Identify the blood parasite species.
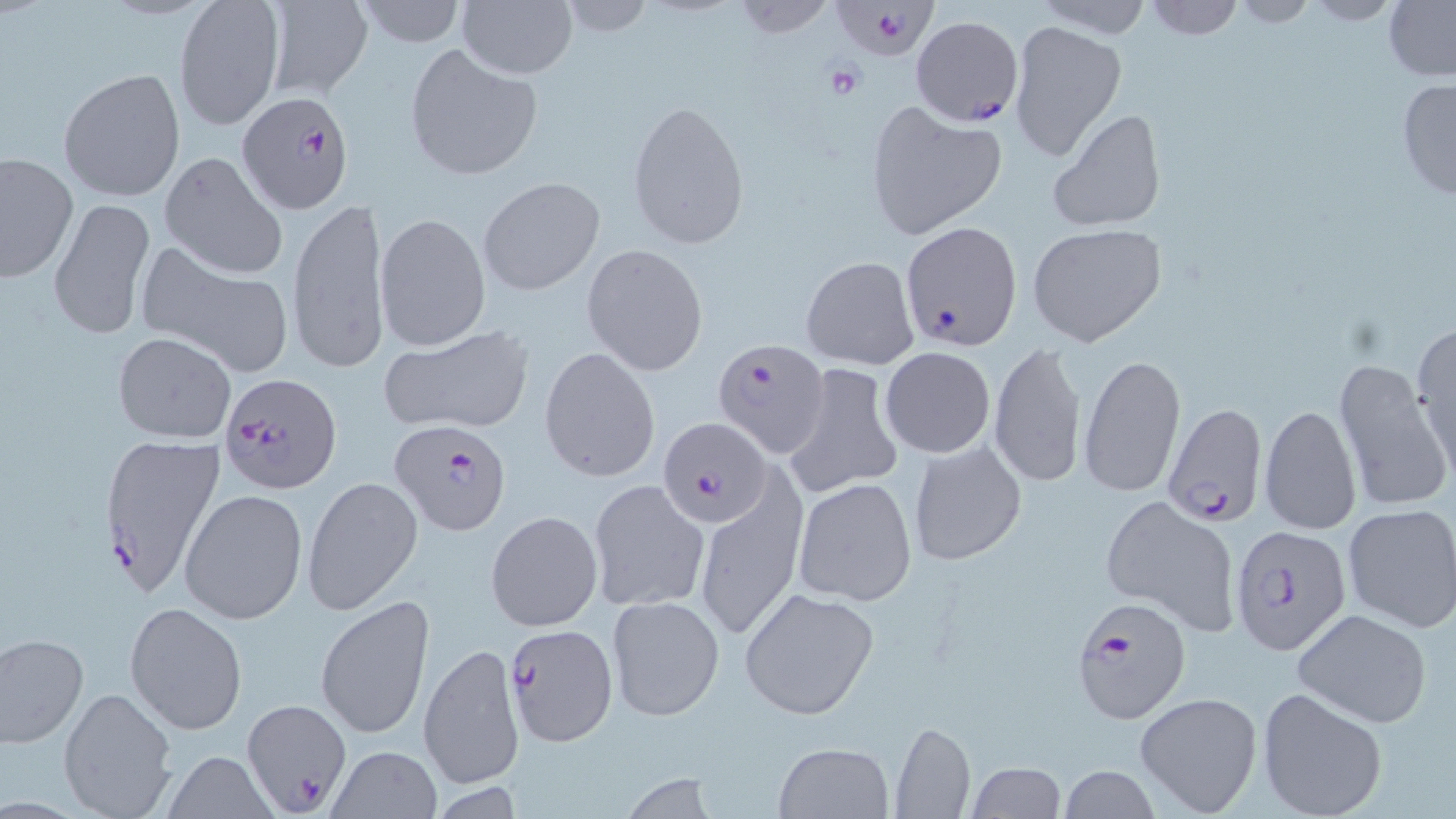
Plasmodium falciparum.

Approximate bounding boxes as (x1, y1, x2, y2) in pixels. Uninfected red blood cell locations: (174, 0, 285, 131), (263, 0, 374, 100), (352, 0, 469, 48), (556, 0, 657, 37), (728, 0, 838, 39), (1031, 0, 1154, 37), (1141, 0, 1246, 40), (459, 1, 576, 78), (1229, 1, 1323, 27), (1299, 1, 1409, 26), (1382, 1, 1456, 82), (1008, 19, 1126, 161), (404, 44, 542, 181), (58, 67, 186, 201), (1394, 78, 1456, 203), (627, 98, 750, 251), (863, 104, 1008, 240), (1048, 108, 1168, 232), (160, 151, 288, 280), (0, 153, 77, 284), (479, 175, 605, 297), (287, 195, 389, 373), (49, 200, 154, 339), (374, 212, 490, 351), (1027, 223, 1167, 347), (134, 241, 297, 376), (581, 243, 709, 375), (800, 255, 919, 370), (1412, 321, 1456, 480), (378, 325, 535, 436), (111, 332, 236, 443), (989, 341, 1087, 488), (539, 346, 660, 483), (879, 347, 996, 459), (1079, 353, 1186, 498), (1332, 359, 1449, 517), (785, 363, 905, 501), (1260, 404, 1362, 536), (907, 440, 1026, 567), (302, 475, 423, 617), (695, 476, 807, 643), (588, 478, 711, 613), (794, 478, 917, 605), (180, 488, 309, 627), (1099, 493, 1241, 636), (1342, 503, 1456, 632), (484, 510, 602, 631), (740, 588, 880, 720), (315, 593, 435, 741), (607, 596, 724, 720), (125, 601, 247, 737), (1290, 608, 1435, 728), (0, 632, 88, 748), (418, 641, 525, 790), (58, 687, 180, 818), (1255, 687, 1389, 819), (1134, 691, 1263, 817), (891, 720, 976, 819), (773, 741, 894, 818), (326, 746, 442, 819), (158, 751, 284, 818), (968, 762, 1066, 818), (1058, 764, 1160, 819). Plasmodium falciparum-infected red blood cell locations: (832, 0, 937, 61), (910, 15, 1023, 126), (236, 92, 354, 215), (900, 221, 1022, 352), (712, 339, 833, 458), (219, 374, 344, 494), (1162, 401, 1265, 525), (658, 416, 771, 530), (387, 421, 513, 535), (97, 431, 226, 602), (1232, 525, 1352, 654), (1070, 597, 1193, 726), (506, 623, 618, 747), (242, 698, 351, 811). Platelet locations: (823, 63, 865, 100). Thin blood film. 1000x magnification. Image is 1456×819 pixels. May-Grünwald-Giemsa stain. Single field of view. Optical microscopy.